Assess the morphology of the red blood cells.
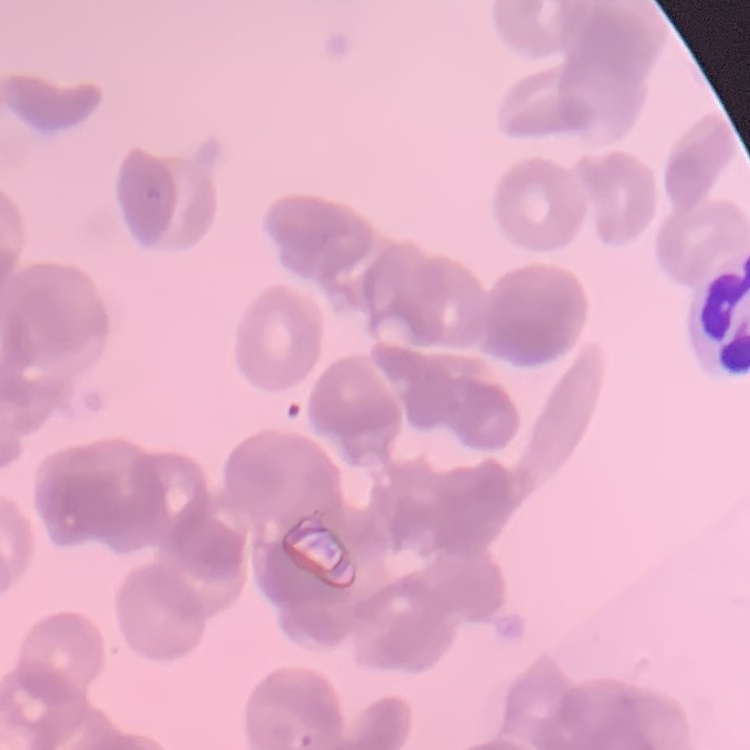
Rouleaux formation.

preparation = thin blood smear
stain = Field's or Giemsa
image type = one tile cut from a larger photomicrograph